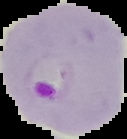

Summary:
  - Image size: 127×139 pixels
  - Image type: segmented cell region with the area outside set to black
  - Preparation: thin blood film
  - Result: Plasmodium parasites identified